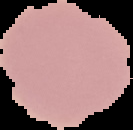
Summary:
  - Image type: cell region segmented out of the field of view; surrounding area masked to black
  - Image size: 133×130 pixels
  - Preparation: thin blood smear
  - Malaria status: uninfected